Give the extent of all uninfected red blood cells.
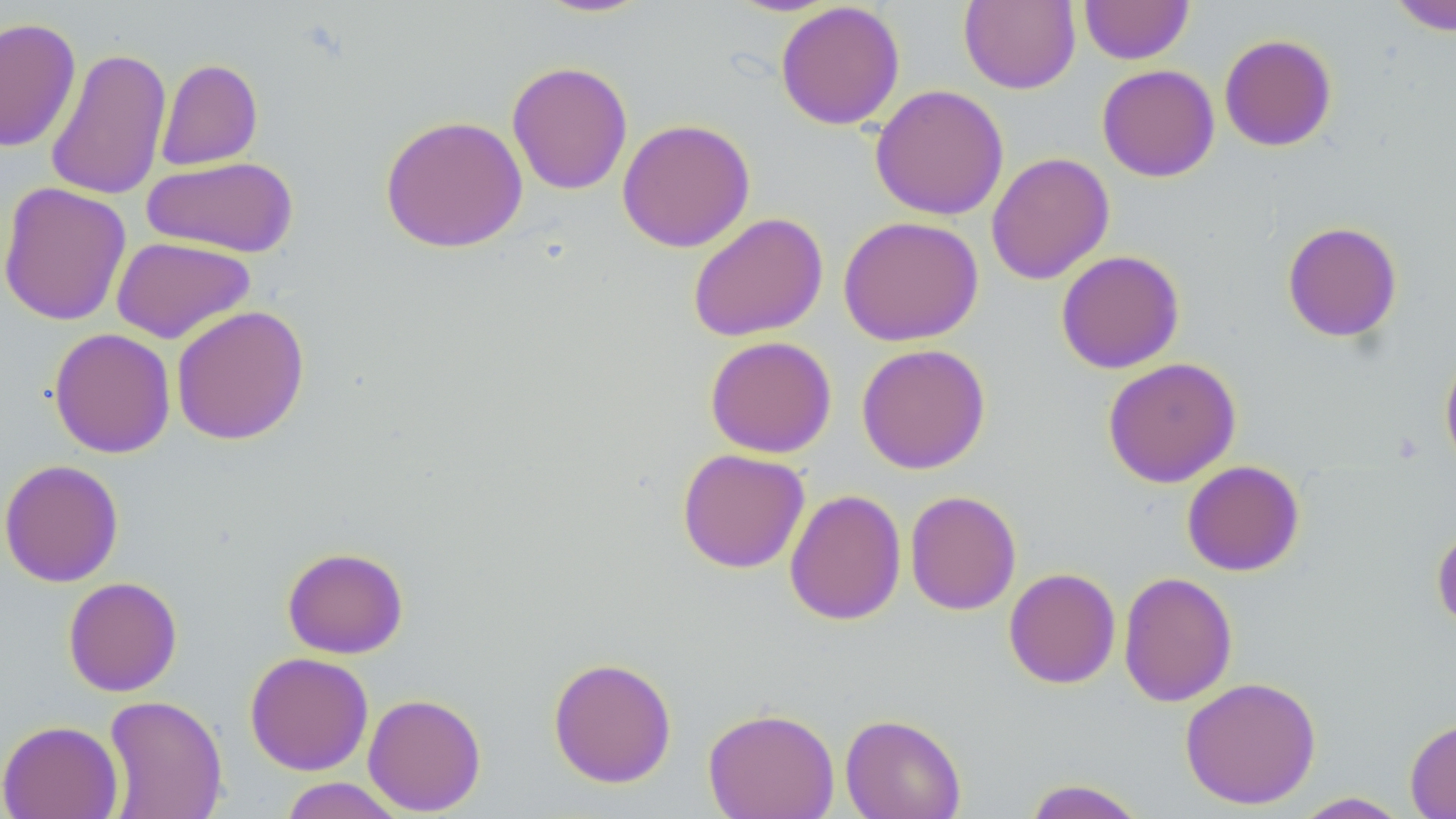

Approximate bounding boxes as [x1, y1, x2, y2] in pixels.
Uninfected red blood cells: [532, 0, 655, 18], [1080, 0, 1193, 64], [1385, 0, 1456, 36], [775, 1, 905, 130], [959, 1, 1080, 94], [0, 17, 82, 153], [1219, 33, 1337, 152], [45, 46, 172, 201], [155, 58, 263, 171], [506, 61, 633, 195], [1097, 64, 1220, 182], [869, 84, 1009, 221], [380, 114, 528, 253], [617, 118, 755, 253], [986, 152, 1115, 285], [142, 156, 299, 257], [0, 181, 132, 326], [686, 212, 828, 342], [838, 215, 984, 346], [1281, 221, 1403, 343], [112, 236, 256, 344], [1055, 250, 1185, 374], [170, 304, 310, 446], [48, 327, 176, 459], [705, 335, 837, 458], [856, 343, 991, 474], [1439, 347, 1456, 475], [1102, 357, 1241, 488], [677, 448, 810, 573], [0, 459, 124, 588], [1181, 460, 1305, 577], [784, 488, 906, 626], [904, 490, 1021, 615], [1431, 523, 1456, 632], [282, 547, 409, 659], [1003, 567, 1121, 689], [1118, 571, 1238, 708], [63, 576, 182, 697], [244, 651, 374, 776], [548, 656, 677, 788], [1180, 676, 1322, 810], [362, 693, 487, 816], [103, 695, 228, 819], [702, 706, 840, 819], [840, 713, 966, 819], [1405, 716, 1456, 819], [1, 719, 123, 819], [277, 777, 408, 818], [1021, 778, 1150, 819], [1291, 792, 1411, 818].

slide-level diagnosis = no evidence of blood parasites
magnification = 1000x
image size = 1456×819 pixels
preparation = thin blood smear
stain = May-Grünwald-Giemsa
modality = optical microscopy
field of view = single